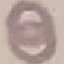

malaria status = uninfected
image type = automatically extracted cell patch, resized to 64 × 64 pixels
stain = Giemsa
preparation = thin blood film
capture = smartphone camera at the microscope eyepiece